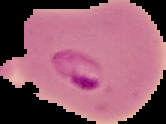

preparation = thin blood film
image size = 166×124 pixels
malaria status = parasitized
image type = cell region segmented out of the field of view; surrounding area masked to black